Give a bounding box for every malaria parasite.
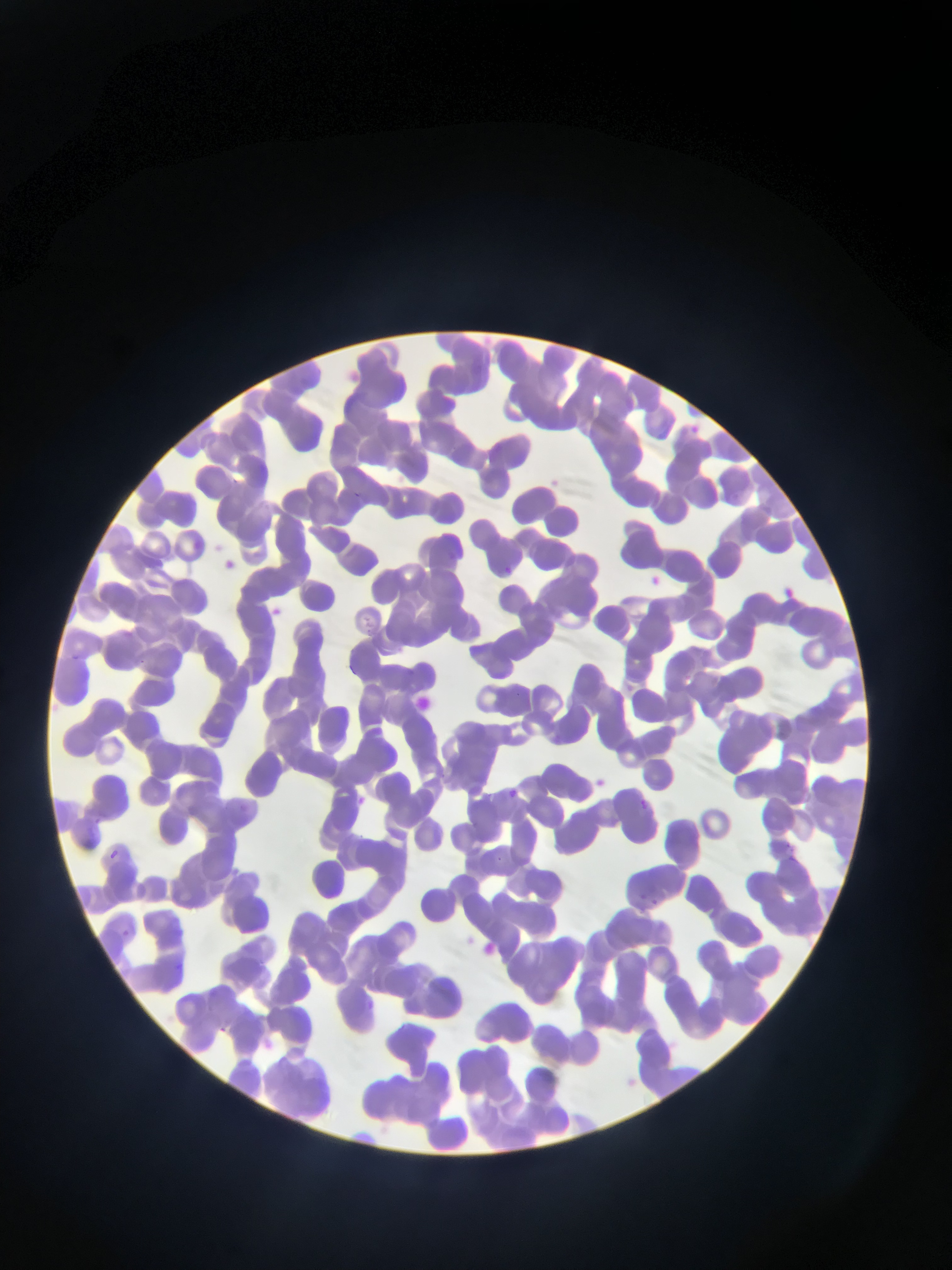
Approximate bounding boxes as (left, top, right, bottom) in pixels.
Malaria parasites: (639, 797, 648, 808), (785, 842, 798, 853), (112, 848, 119, 859), (495, 855, 504, 863), (122, 932, 131, 938) | approximate (x, y) pixel centers of objects too small to bound: (656, 902).

One field of view. Sample from Ghana. Image is 952×1270 pixels. Thin blood film. Photographed through a microscope with a mobile-phone camera.